Classify this cell by malaria status.
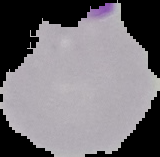
Parasitized.

Cell region segmented out of the field of view; the surrounding area is masked to black. Image is 160×157 pixels. From a thin blood film.